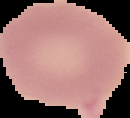 Image is 130×118 pixels. Malaria status: uninfected. From a thin blood smear. The area outside the segmented cell region is set to black.